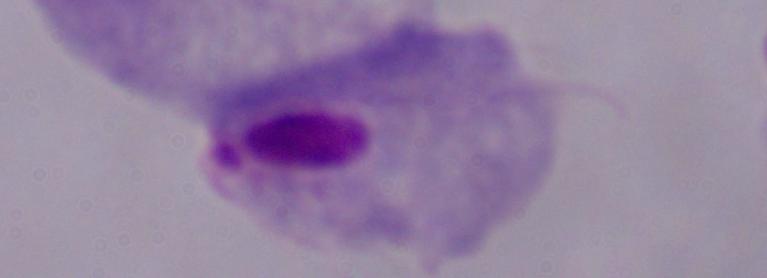

Photomicrograph. A trichomonad is seen. 1000x magnification.